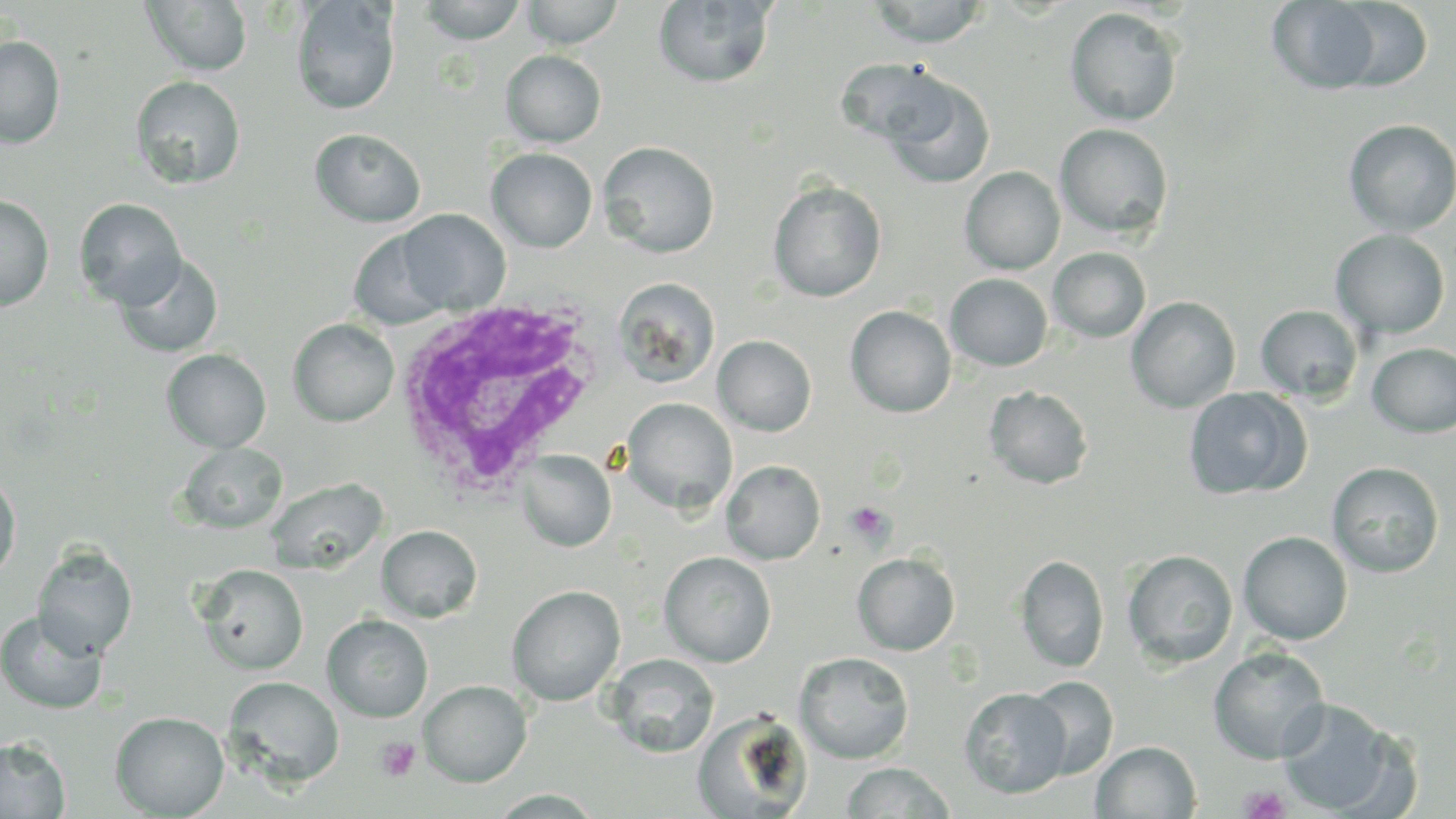

Summary:
  - Coordinate format: approximate bounding boxes as (x1,y1)-(x2,y2) corner pairs in pixels
  - White blood cell locations: (390,298)-(610,500)
  - Platelet locations: (846,501)-(894,546), (375,736)-(421,783), (1240,786)-(1289,819)
  - Uninfected red blood cell locations: (292,0)-(400,116), (419,0)-(527,45), (520,0)-(625,48), (867,0)-(989,47), (1333,0)-(1432,91), (143,1)-(253,76), (653,1)-(776,89), (1267,1)-(1382,94), (1065,7)-(1183,126), (0,36)-(65,148), (500,50)-(606,147), (836,56)-(951,147), (131,76)-(245,190), (884,76)-(995,190), (1343,119)-(1456,236), (1055,124)-(1173,238), (310,129)-(427,228), (598,141)-(720,258), (487,148)-(597,252), (960,166)-(1065,275), (768,180)-(886,302), (0,194)-(54,311), (75,199)-(185,310), (396,209)-(511,315), (349,228)-(453,330), (1331,229)-(1450,339), (1048,247)-(1151,343), (115,253)-(223,359), (945,273)-(1053,371), (612,276)-(721,389), (1126,296)-(1240,413), (1256,305)-(1363,402), (845,306)-(956,417), (288,318)-(399,427), (713,335)-(817,436), (1367,343)-(1456,437), (162,349)-(271,453), (984,386)-(1093,489), (1183,387)-(1311,500), (621,398)-(738,515), (177,442)-(287,534), (516,450)-(616,552), (722,460)-(825,564), (1327,462)-(1444,577), (0,472)-(21,582), (265,477)-(388,574), (376,525)-(482,622), (1238,531)-(1353,645), (33,545)-(137,660), (1122,549)-(1238,669), (659,551)-(776,667), (852,552)-(960,655), (1015,553)-(1109,673), (195,564)-(308,674), (507,585)-(625,706), (0,612)-(107,715), (322,614)-(433,722), (1209,646)-(1330,764), (794,651)-(914,764), (606,653)-(719,758), (223,676)-(344,788), (1024,676)-(1119,779), (419,680)-(533,787), (960,687)-(1071,798), (1276,699)-(1406,816), (110,710)-(229,818), (692,711)-(812,819), (0,737)-(69,819), (1091,741)-(1201,818), (840,761)-(957,818)
  - Slide-level diagnosis: Plasmodium ovale
  - Magnification: 1000x
  - Image size: 1456×819 pixels
  - Field of view: one of a larger specimen
  - Stain: May-Grünwald-Giemsa
  - Preparation: thin blood smear
  - Modality: optical microscopy